Comment on the morphology of the erythrocytes.
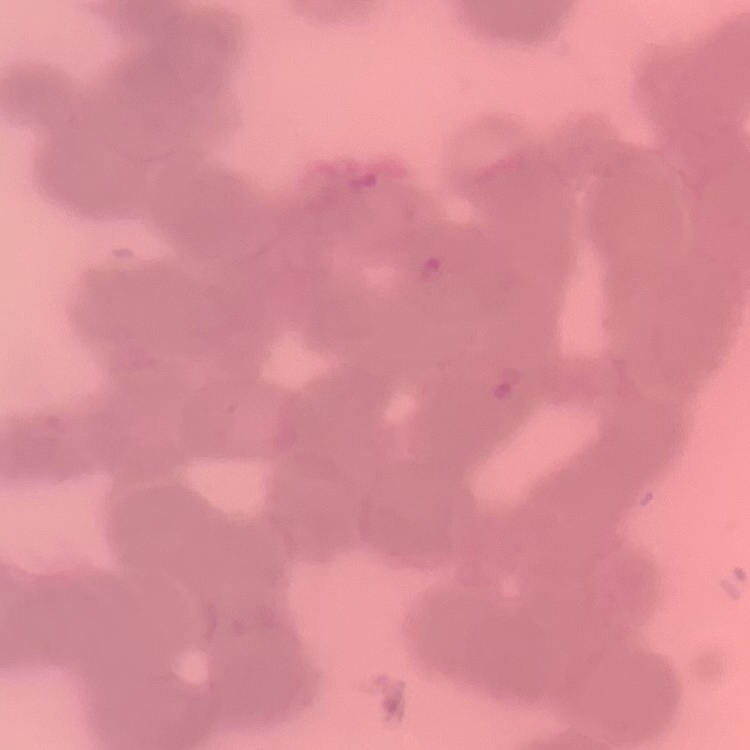
They show rouleaux formation.

Summary:
  - Image type: square crop of a larger photomicrograph
  - Stain: Field's or Giemsa
  - Preparation: thin blood film